State which parasite is depicted.
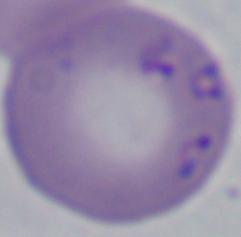

Babesia.

Photomicrograph. 1000x magnification.